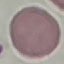 Result: no malaria parasites seen. Giemsa-stained preparation. Acquired by smartphone through the microscope eyepiece. Thin smear of blood. Automatically extracted cell patch, resized to 64 × 64 pixels.